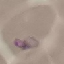
{
  "result": "malaria parasites identified",
  "stain": "Giemsa",
  "image_type": "cell patch, automatically extracted from a larger field of view and resized to 64 × 64 pixels",
  "preparation": "thin blood film",
  "capture": "smartphone camera at the microscope eyepiece"
}